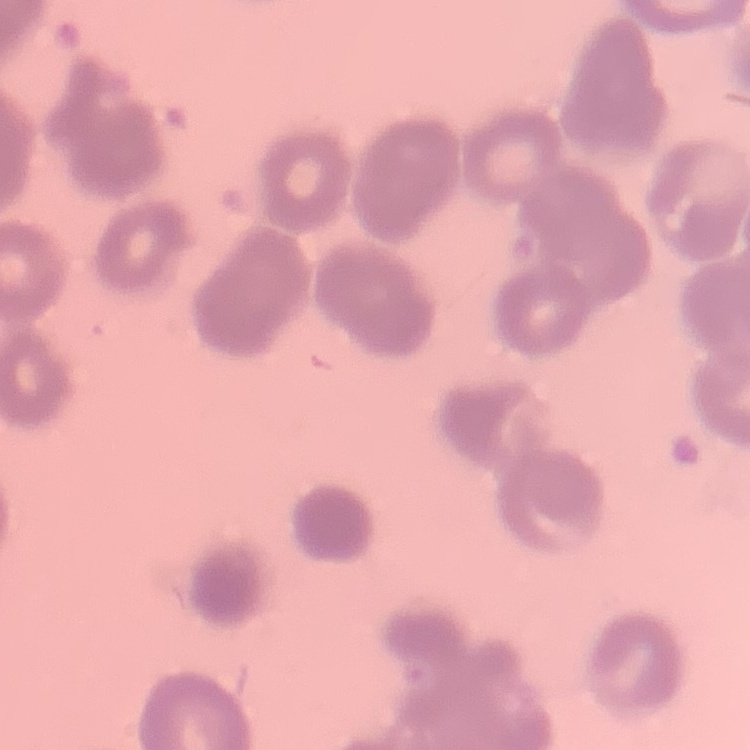

The erythrocytes show rouleaux formation. Thin peripheral smear. Square crop of a larger photomicrograph. Field's or Giemsa stain.